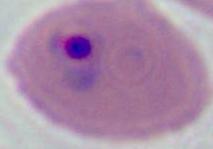
A Plasmodium parasite is seen. Captured at either 400x or 1000x magnification. Micrograph.